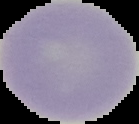
{
  "preparation": "thin blood film",
  "malaria_status": "uninfected",
  "image_size": "139×124 pixels",
  "image_type": "segmented cell region with the area outside set to black"
}